Locate every blood parasite and identify its species.
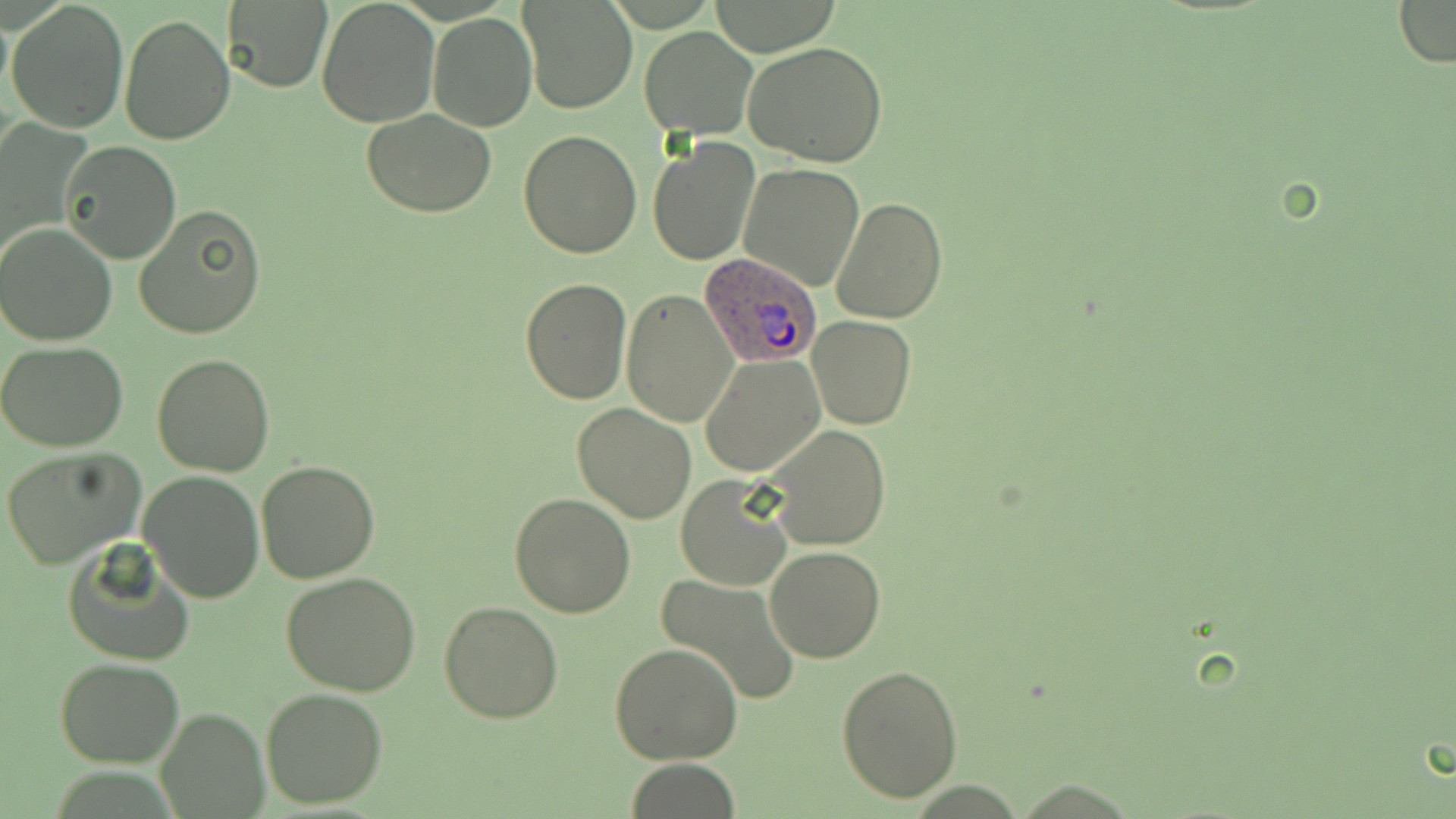

Approximate bounding boxes as named x1/y1/x2/y2 corners in pixels.
Plasmodium ovale-infected red blood cells: (x1=696, y1=251, x2=826, y2=369).
No Plasmodium falciparum, Plasmodium malariae, Plasmodium vivax, Babesia divergens, or Trypanosoma brucei observed.

Uninfected red blood cell locations: (x1=317, y1=0, x2=439, y2=127), (x1=519, y1=0, x2=638, y2=115), (x1=1391, y1=0, x2=1456, y2=69), (x1=6, y1=1, x2=130, y2=134), (x1=224, y1=2, x2=332, y2=91), (x1=0, y1=6, x2=14, y2=100), (x1=117, y1=11, x2=236, y2=144), (x1=429, y1=12, x2=535, y2=131), (x1=639, y1=26, x2=757, y2=139), (x1=743, y1=41, x2=888, y2=167), (x1=362, y1=109, x2=498, y2=218), (x1=0, y1=121, x2=88, y2=268), (x1=517, y1=129, x2=642, y2=260), (x1=647, y1=136, x2=759, y2=267), (x1=60, y1=142, x2=180, y2=263), (x1=738, y1=163, x2=864, y2=291), (x1=831, y1=198, x2=948, y2=324), (x1=134, y1=202, x2=267, y2=339), (x1=0, y1=222, x2=119, y2=347), (x1=519, y1=279, x2=633, y2=405), (x1=622, y1=289, x2=738, y2=429), (x1=806, y1=315, x2=916, y2=429), (x1=0, y1=343, x2=130, y2=451), (x1=152, y1=354, x2=276, y2=477), (x1=701, y1=356, x2=824, y2=477), (x1=573, y1=403, x2=696, y2=524), (x1=764, y1=425, x2=890, y2=551), (x1=2, y1=447, x2=147, y2=568), (x1=256, y1=461, x2=380, y2=584), (x1=138, y1=472, x2=264, y2=603), (x1=675, y1=473, x2=793, y2=590), (x1=509, y1=493, x2=636, y2=617), (x1=62, y1=541, x2=197, y2=667), (x1=765, y1=545, x2=885, y2=662), (x1=281, y1=572, x2=422, y2=697), (x1=655, y1=573, x2=802, y2=706), (x1=439, y1=599, x2=563, y2=723), (x1=609, y1=642, x2=744, y2=766), (x1=55, y1=658, x2=185, y2=767), (x1=836, y1=663, x2=964, y2=802), (x1=260, y1=689, x2=387, y2=809), (x1=155, y1=706, x2=269, y2=819), (x1=625, y1=759, x2=741, y2=817). Slide-level diagnosis: Plasmodium ovale. Image is 1456×819 pixels. May-Grünwald-Giemsa stain. Thin blood smear. Light microscopy. Single field of view. 1000x magnification.